Classify this cell by malaria status.
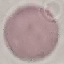
Uninfected.

image_type: automatically extracted cell patch, resized to 64 × 64 pixels
preparation: thin smear
stain: Giemsa
capture: smartphone camera at the microscope eyepiece